Assess the morphology of the erythrocytes.
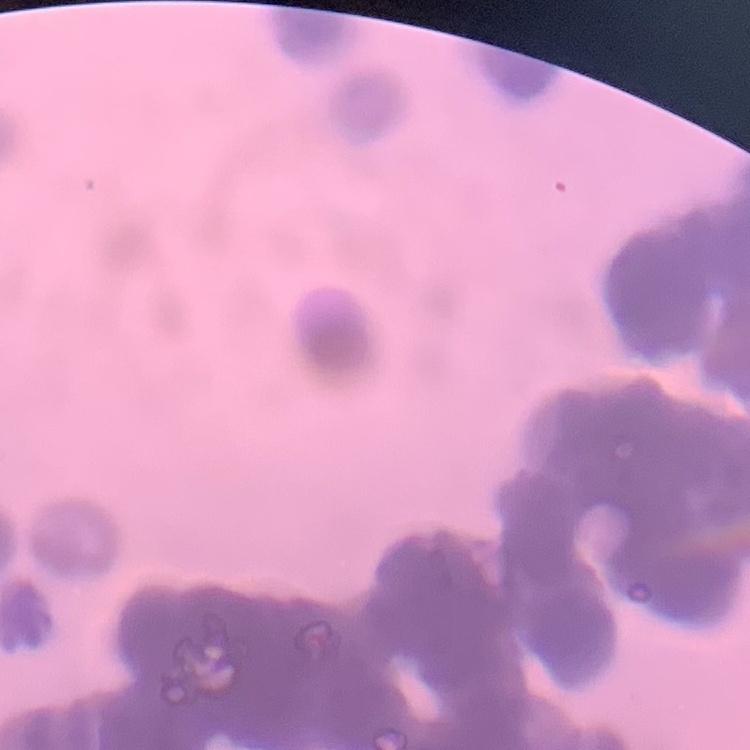
They show rouleaux formation.

Summary:
  - Stain: Field's or Giemsa
  - Preparation: thin peripheral smear
  - Image type: square crop of a larger photomicrograph